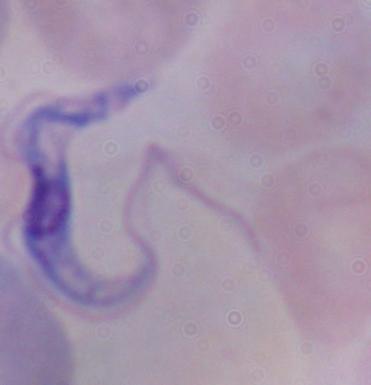

magnification = 1000x
identification = trypanosome
modality = micrograph